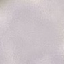 Result: negative for malaria parasites. Thin blood smear. Automatically extracted cell patch, resized to 64 × 64 pixels. Acquired by smartphone through the microscope eyepiece. Giemsa-stained preparation.